Describe the morphology of the red blood cells.
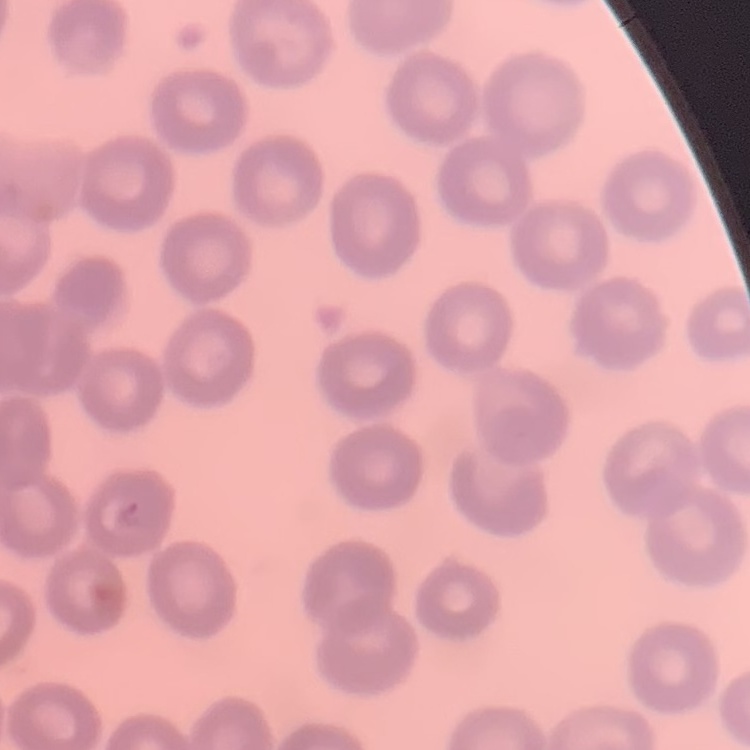

They show no rouleaux formation.

Summary:
  - Image type: square crop of a larger photomicrograph
  - Preparation: thin peripheral smear
  - Stain: Field's or Giemsa